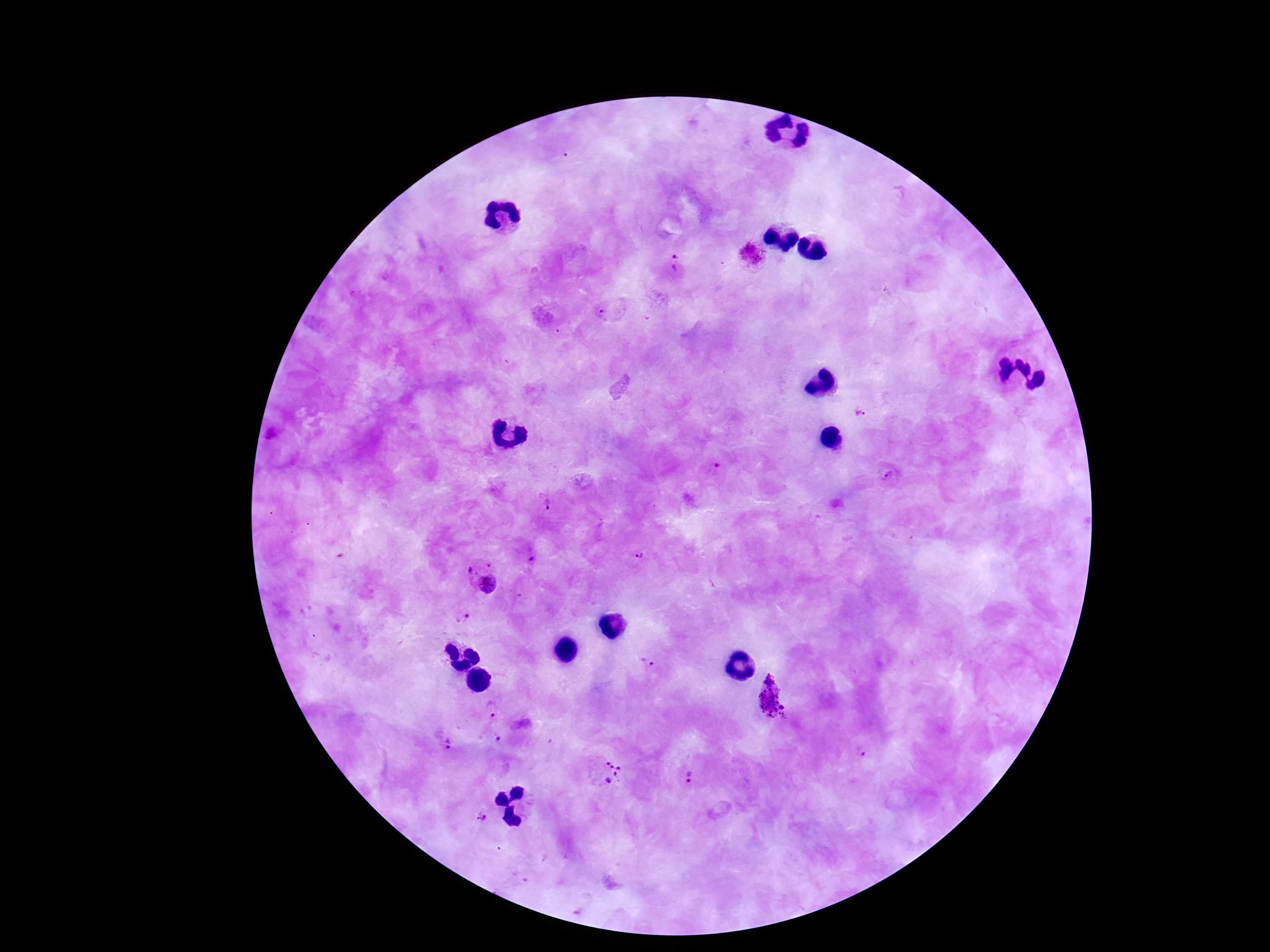

{
  "preparation": "thick peripheral-blood smear",
  "stain": "Giemsa",
  "image_size": "1270×952 pixels",
  "plasmodium_parasite_locations": "approximate centers as {x, y} in pixels: {753, 259}, {673, 265}, {607, 315}, {861, 415}, {713, 469}, {888, 475}, {549, 501}, {641, 554}, {531, 558}, {482, 579}, {461, 616}, {647, 662}, {772, 696}, {494, 710}, {498, 740}, {445, 744}, {612, 772}, {688, 778}, {483, 818}",
  "capture": "smartphone camera through the microscope eyepiece",
  "magnification": "100x",
  "field_of_view": "single",
  "patient_malaria_status": "infected"
}